Locate every Plasmodium vivax-infected red blood cell.
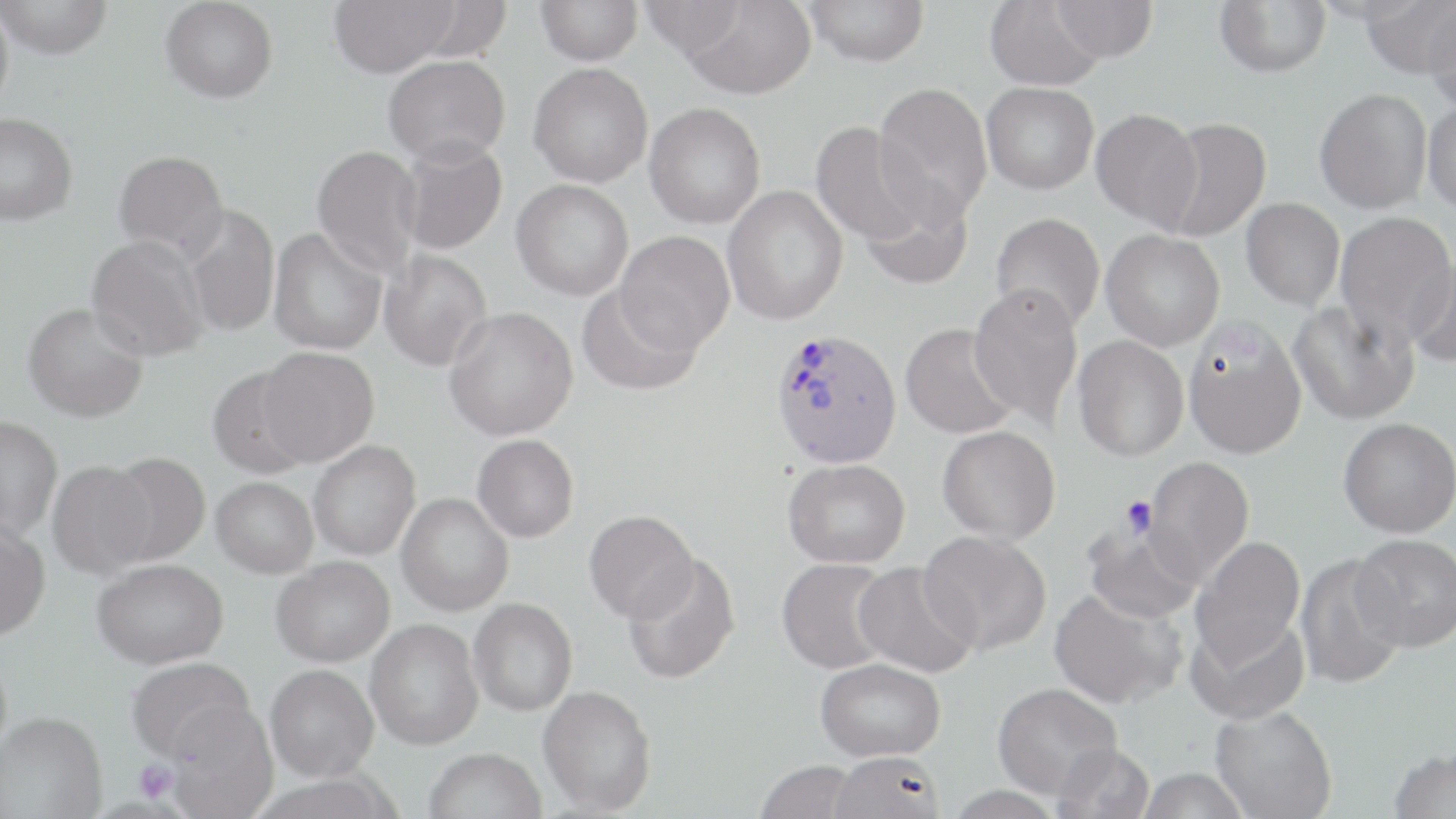
Approximate bounding boxes as named x1/y1/x2/y2 corners in pixels.
Plasmodium vivax-infected red blood cells: (x1=769, y1=328, x2=902, y2=468).

Summary:
  - Uninfected red blood cell locations: (x1=0, y1=0, x2=14, y2=117), (x1=0, y1=0, x2=114, y2=59), (x1=161, y1=0, x2=278, y2=103), (x1=328, y1=0, x2=458, y2=77), (x1=536, y1=0, x2=643, y2=65), (x1=804, y1=0, x2=929, y2=66), (x1=1051, y1=0, x2=1158, y2=63), (x1=1214, y1=0, x2=1331, y2=77), (x1=1359, y1=0, x2=1456, y2=80), (x1=639, y1=1, x2=746, y2=56), (x1=679, y1=1, x2=817, y2=100), (x1=985, y1=1, x2=1105, y2=90), (x1=1423, y1=5, x2=1456, y2=117), (x1=383, y1=54, x2=510, y2=165), (x1=528, y1=62, x2=653, y2=187), (x1=981, y1=81, x2=1098, y2=194), (x1=873, y1=83, x2=993, y2=223), (x1=1314, y1=88, x2=1432, y2=214), (x1=1422, y1=100, x2=1456, y2=214), (x1=644, y1=102, x2=766, y2=229), (x1=1091, y1=108, x2=1203, y2=231), (x1=0, y1=113, x2=78, y2=226), (x1=1157, y1=116, x2=1272, y2=242), (x1=811, y1=120, x2=932, y2=247), (x1=397, y1=137, x2=508, y2=256), (x1=311, y1=144, x2=424, y2=279), (x1=113, y1=150, x2=229, y2=263), (x1=511, y1=179, x2=633, y2=301), (x1=858, y1=182, x2=975, y2=291), (x1=723, y1=185, x2=848, y2=325), (x1=1241, y1=198, x2=1344, y2=311), (x1=182, y1=205, x2=279, y2=338), (x1=990, y1=213, x2=1105, y2=332), (x1=1335, y1=213, x2=1456, y2=344), (x1=268, y1=226, x2=388, y2=355), (x1=1101, y1=229, x2=1225, y2=351), (x1=616, y1=230, x2=734, y2=353), (x1=85, y1=234, x2=211, y2=362), (x1=378, y1=249, x2=492, y2=371), (x1=1405, y1=252, x2=1456, y2=369), (x1=577, y1=284, x2=702, y2=397), (x1=968, y1=284, x2=1083, y2=427), (x1=1288, y1=298, x2=1420, y2=426), (x1=23, y1=302, x2=149, y2=422), (x1=444, y1=306, x2=578, y2=441), (x1=1183, y1=320, x2=1308, y2=460), (x1=900, y1=323, x2=1019, y2=439), (x1=1073, y1=335, x2=1189, y2=461), (x1=258, y1=346, x2=380, y2=466), (x1=206, y1=366, x2=315, y2=480), (x1=0, y1=416, x2=63, y2=540), (x1=1339, y1=417, x2=1456, y2=537), (x1=937, y1=426, x2=1060, y2=544), (x1=472, y1=434, x2=579, y2=542), (x1=308, y1=440, x2=421, y2=561), (x1=103, y1=452, x2=211, y2=566), (x1=1140, y1=457, x2=1255, y2=586), (x1=783, y1=458, x2=910, y2=568), (x1=47, y1=460, x2=157, y2=579), (x1=211, y1=477, x2=319, y2=578), (x1=396, y1=493, x2=514, y2=616), (x1=584, y1=510, x2=699, y2=623), (x1=0, y1=520, x2=51, y2=640), (x1=1082, y1=520, x2=1205, y2=624), (x1=919, y1=530, x2=1052, y2=656), (x1=1351, y1=533, x2=1456, y2=651), (x1=1190, y1=536, x2=1306, y2=670), (x1=1294, y1=552, x2=1409, y2=691), (x1=622, y1=553, x2=741, y2=685), (x1=271, y1=556, x2=395, y2=667), (x1=777, y1=557, x2=895, y2=674), (x1=92, y1=558, x2=228, y2=669), (x1=853, y1=562, x2=978, y2=678), (x1=1049, y1=587, x2=1187, y2=710), (x1=469, y1=598, x2=578, y2=716), (x1=1187, y1=612, x2=1310, y2=725), (x1=365, y1=619, x2=484, y2=750), (x1=126, y1=656, x2=256, y2=765), (x1=816, y1=657, x2=946, y2=761), (x1=265, y1=664, x2=379, y2=782), (x1=993, y1=682, x2=1123, y2=801), (x1=537, y1=685, x2=657, y2=814), (x1=164, y1=703, x2=279, y2=819), (x1=1210, y1=704, x2=1338, y2=819), (x1=0, y1=712, x2=107, y2=818), (x1=1052, y1=742, x2=1155, y2=819), (x1=1387, y1=746, x2=1455, y2=818), (x1=423, y1=748, x2=546, y2=819), (x1=829, y1=750, x2=944, y2=819), (x1=755, y1=760, x2=859, y2=819), (x1=1135, y1=767, x2=1253, y2=818)
  - Platelet locations: (x1=1121, y1=495, x2=1158, y2=537), (x1=135, y1=759, x2=179, y2=804)
  - Slide-level diagnosis: Plasmodium vivax
  - Preparation: thin blood film
  - Modality: light microscopy
  - Stain: May-Grünwald-Giemsa
  - Magnification: 1000x
  - Field of view: one of a larger specimen
  - Image size: 1456×819 pixels